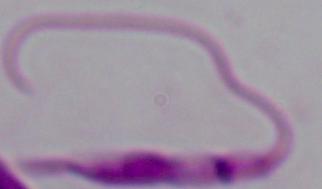
magnification = 1000x
modality = micrograph
identification = Leishmania